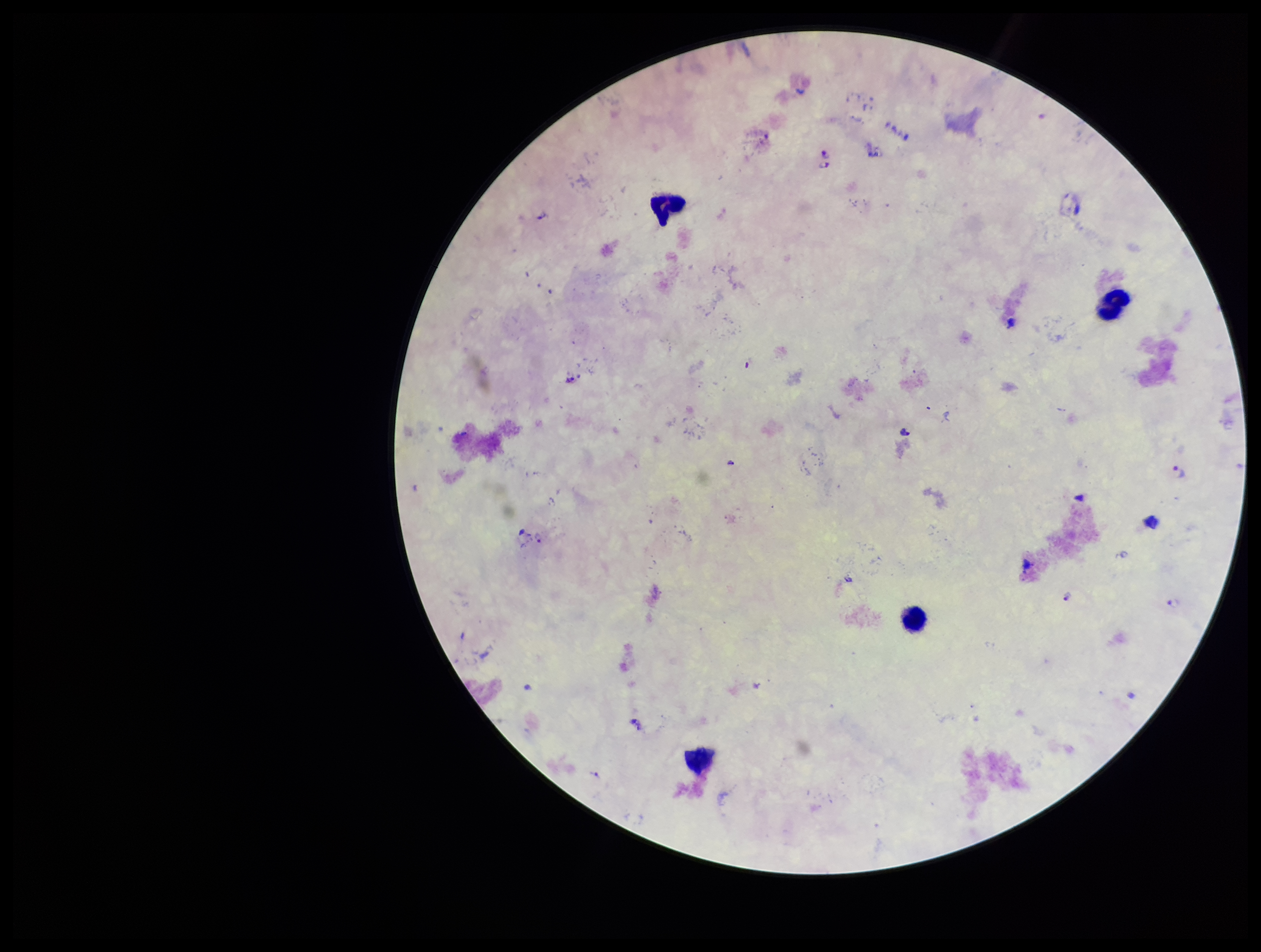
Summary:
  - Image size: 1261×952 pixels
  - Patient malaria status: infected
  - Plasmodium parasites: identified
  - Preparation: thick smear
  - Parasite count: 8
  - Capture: smartphone photograph through the microscope eyepiece
  - Field of view: single
  - Stain: Giemsa
  - Leukocyte count: 4
  - Species reported for this patient: Plasmodium falciparum